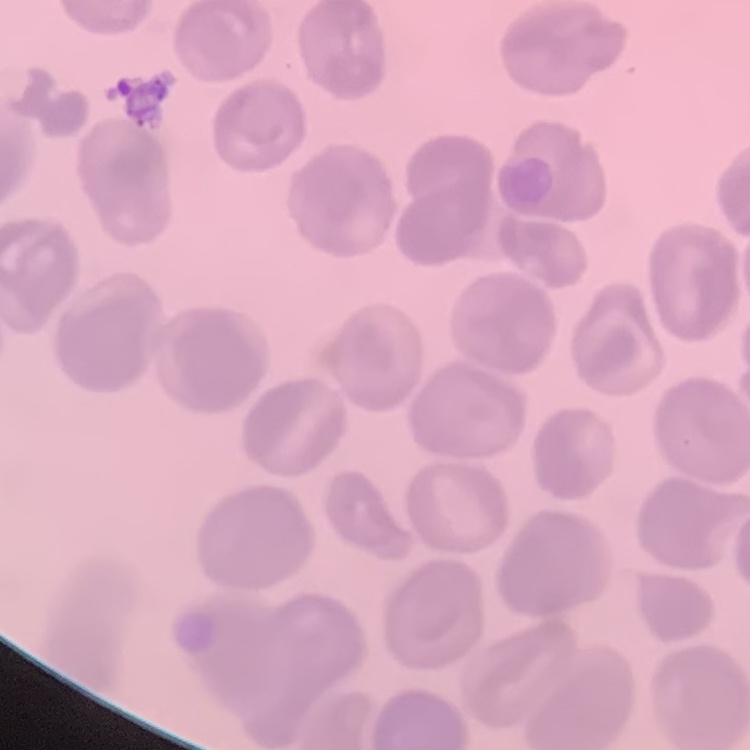
Summary:
  - Red blood cell morphology: no rouleaux formation
  - Preparation: thin blood film
  - Image type: square crop of a larger photomicrograph
  - Stain: Field's or Giemsa